Assess this cell for malaria.
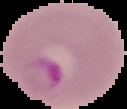
Parasitized.

Summary:
  - Image size: 127×109 pixels
  - Preparation: thin blood film
  - Image type: cell region segmented out of the field of view; surrounding area masked to black